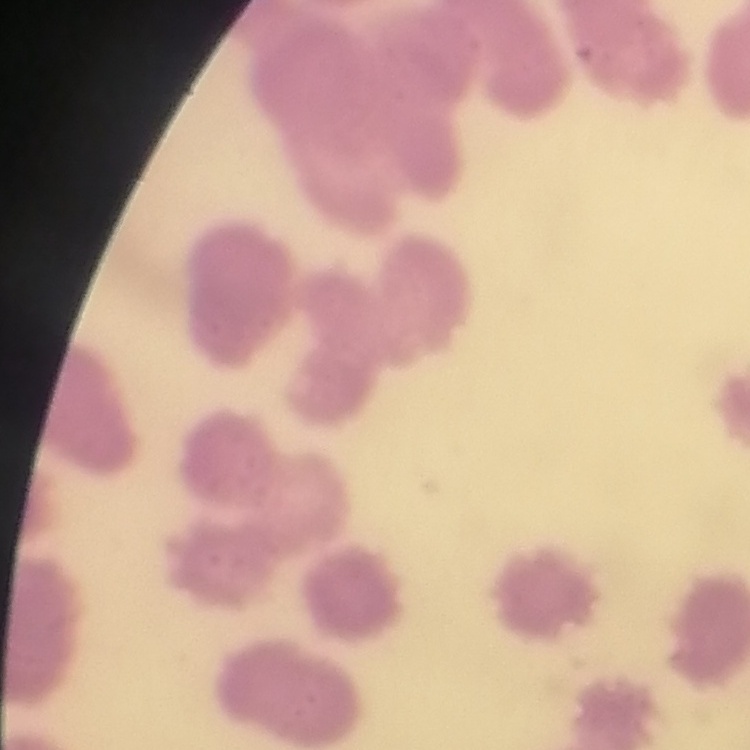

Summary:
  - Red blood cell morphology: rouleaux formation
  - Stain: Field's or Giemsa
  - Image type: one tile cut from a larger photomicrograph
  - Preparation: thin peripheral smear